Report the malaria status of this cell.
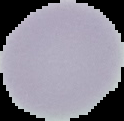

It is uninfected.

Summary:
  - Preparation: thin blood smear
  - Image size: 124×121 pixels
  - Image type: cell region segmented out of the field of view; surrounding area masked to black